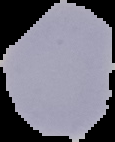 Malaria status: uninfected. Image is 115×142 pixels. Cell region segmented out of the field of view; the surrounding area is masked to black. From a thin blood smear.